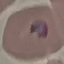

Malaria status: parasitized. Thin blood film. Giemsa stain. Acquired by smartphone through the microscope eyepiece. Cell patch, automatically extracted from a larger field of view and resized to 64 × 64 pixels.